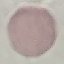
Summary:
  - Malaria status: uninfected
  - Image type: automatically extracted cell patch, resized to 64 × 64 pixels
  - Stain: Giemsa
  - Preparation: thin blood smear
  - Capture: smartphone through the microscope eyepiece